Look for Plasmodium parasites.
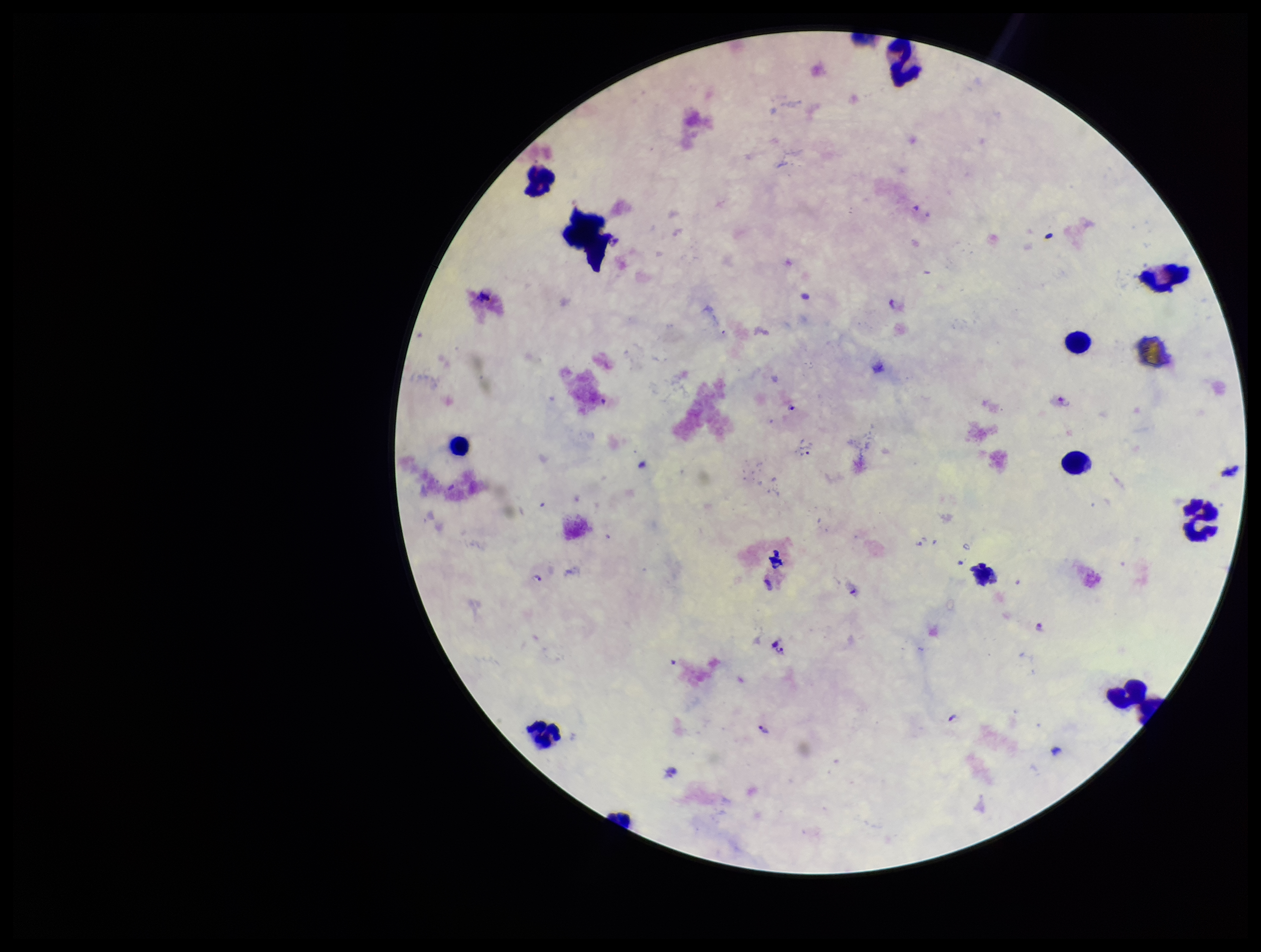

Identified.

Species reported for this patient: Plasmodium falciparum. Patient malaria status: positive. Leukocyte count: 12. Preparation: thick smear. Parasite count: 4. Stained with Giemsa. Smartphone photograph taken through the eyepiece of a microscope. One field from this slide. Image is 1261×952 pixels.